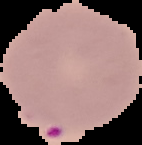
image size = 142×145 pixels
malaria status = parasitized
preparation = thin blood smear
image type = segmented cell region with the area outside set to black